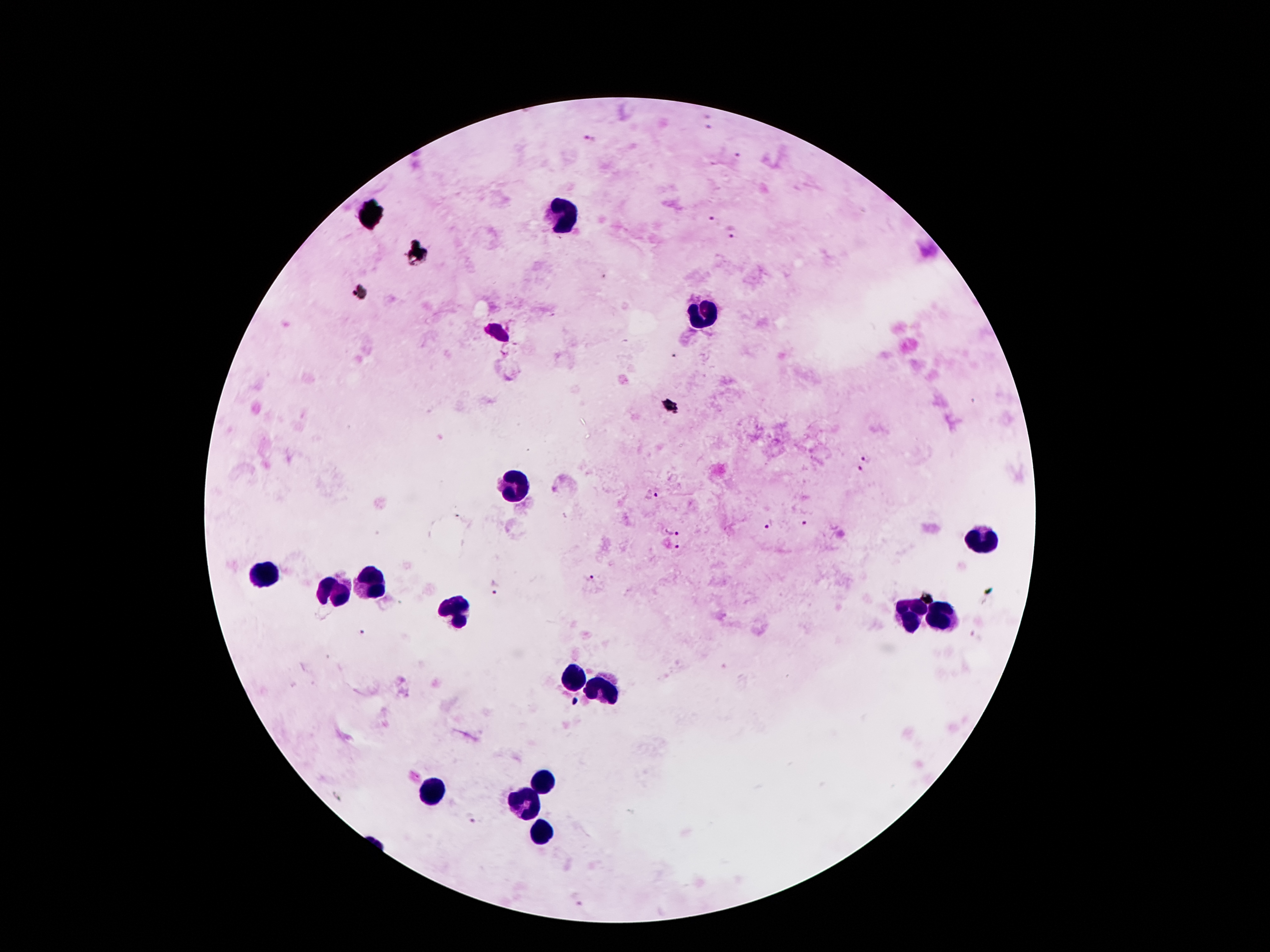
{
  "plasmodium_parasite_locations": "approximate centers as (x, y) in pixels: (708, 126), (592, 141), (737, 155), (712, 221), (734, 232), (866, 458), (859, 471), (659, 494), (801, 524), (770, 527), (674, 529), (679, 547), (590, 579), (493, 588), (364, 635), (471, 818)",
  "capture": "smartphone camera through the microscope eyepiece",
  "image_size": "1270×952 pixels",
  "stain": "Giemsa",
  "patient_malaria_status": "infected with Plasmodium falciparum",
  "magnification": "100x",
  "preparation": "thick blood smear",
  "field_of_view": "one from this slide",
  "leukocyte_locations": "approximate centers as (x, y) in pixels: (566, 212), (372, 217), (703, 314), (519, 486), (985, 540), (267, 572), (365, 583), (331, 591), (912, 611), (453, 612), (944, 617), (572, 682), (599, 696), (544, 777), (431, 793), (524, 800), (539, 836)"
}